Outline each blood parasite and name the species.
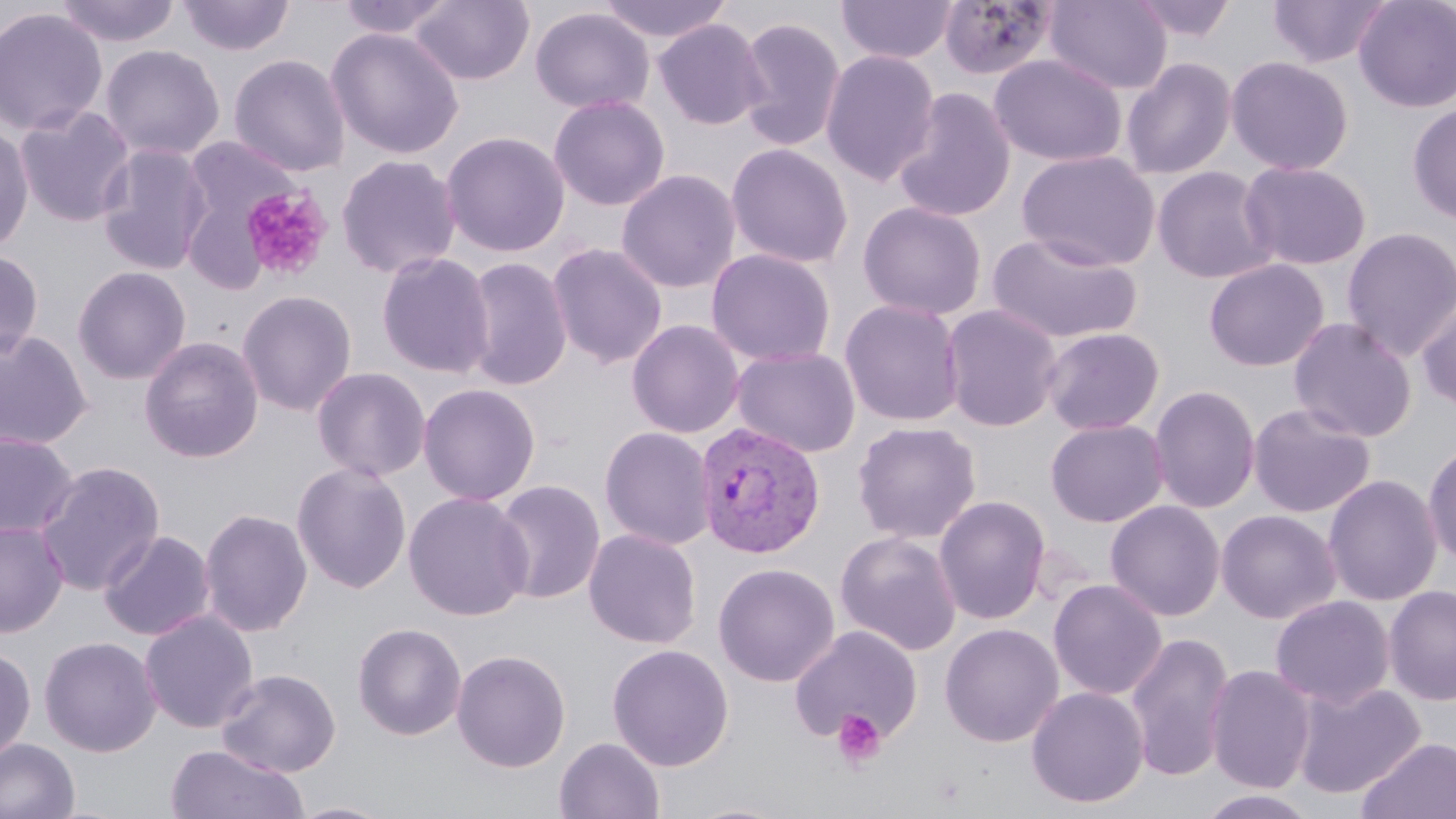

Approximate bounding boxes as [x1, y1, x2, y2] in pixels.
Plasmodium vivax-infected red blood cells: [693, 421, 826, 559].
No Plasmodium falciparum, Plasmodium ovale, Plasmodium malariae, Babesia divergens, or Trypanosoma brucei observed.

Summary:
  - Platelet locations: [239, 187, 333, 283], [831, 708, 886, 769]
  - Uninfected red blood cell locations: [52, 0, 183, 48], [177, 0, 296, 57], [335, 0, 456, 40], [410, 0, 535, 86], [597, 0, 734, 44], [835, 0, 958, 65], [1044, 0, 1173, 94], [1127, 0, 1240, 44], [1267, 0, 1393, 69], [1353, 0, 1456, 113], [938, 1, 1059, 82], [0, 7, 108, 137], [530, 7, 654, 114], [735, 15, 847, 152], [653, 18, 768, 130], [326, 27, 465, 160], [99, 44, 226, 161], [820, 49, 940, 186], [228, 53, 351, 176], [988, 54, 1128, 167], [1224, 56, 1355, 175], [1120, 57, 1237, 179], [893, 86, 1017, 222], [548, 94, 670, 211], [1407, 102, 1456, 225], [13, 104, 138, 228], [0, 122, 35, 254], [440, 131, 571, 258], [183, 135, 304, 236], [96, 143, 214, 275], [726, 143, 853, 269], [1016, 150, 1162, 271], [335, 154, 462, 280], [1239, 160, 1372, 271], [1151, 166, 1279, 284], [616, 169, 742, 294], [857, 201, 988, 320], [1340, 226, 1456, 361], [986, 230, 1145, 345], [546, 243, 668, 369], [706, 248, 837, 367], [0, 249, 44, 361], [375, 251, 495, 379], [462, 255, 573, 392], [1204, 258, 1329, 372], [72, 266, 191, 384], [237, 289, 357, 416], [1416, 294, 1456, 412], [839, 298, 966, 427], [940, 304, 1064, 432], [1287, 316, 1418, 442], [626, 319, 746, 439], [1040, 326, 1165, 435], [0, 328, 93, 451], [138, 335, 264, 463], [730, 346, 861, 458], [311, 366, 431, 482], [417, 383, 541, 506], [1148, 384, 1261, 514], [1248, 402, 1376, 518], [1045, 418, 1169, 527], [851, 421, 982, 544], [599, 426, 717, 550], [0, 432, 79, 539], [1423, 440, 1456, 569], [35, 460, 166, 596], [291, 461, 412, 594], [1323, 473, 1443, 606], [492, 479, 606, 606], [403, 491, 534, 621], [934, 495, 1051, 624], [1104, 499, 1225, 621], [199, 507, 313, 638], [1216, 509, 1341, 624], [0, 519, 68, 637], [583, 528, 703, 649], [98, 529, 216, 641], [834, 530, 963, 656], [712, 562, 840, 687], [1048, 578, 1167, 701], [1383, 585, 1456, 705], [1270, 594, 1395, 708], [139, 609, 259, 734], [352, 622, 467, 741], [939, 623, 1064, 747], [788, 624, 924, 747], [1124, 631, 1235, 782], [38, 636, 161, 757], [607, 643, 734, 771], [0, 646, 36, 762], [451, 649, 572, 772], [1205, 664, 1317, 794], [215, 668, 341, 778], [1291, 680, 1426, 800], [1026, 685, 1149, 808], [554, 736, 665, 818], [1357, 736, 1456, 819], [0, 737, 80, 819], [165, 743, 308, 819], [1195, 789, 1320, 819], [286, 800, 397, 819], [681, 800, 801, 819]
  - Slide-level diagnosis: Plasmodium vivax
  - Magnification: 1000x
  - Field of view: single
  - Modality: optical microscopy
  - Preparation: thin blood smear
  - Stain: May-Grünwald-Giemsa
  - Image size: 1456×819 pixels